Assess this cell for malaria.
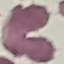
It is uninfected.

stain = Giemsa
capture = smartphone camera at the microscope eyepiece
image type = automatically extracted cell patch, resized to 64 × 64 pixels
preparation = thin smear